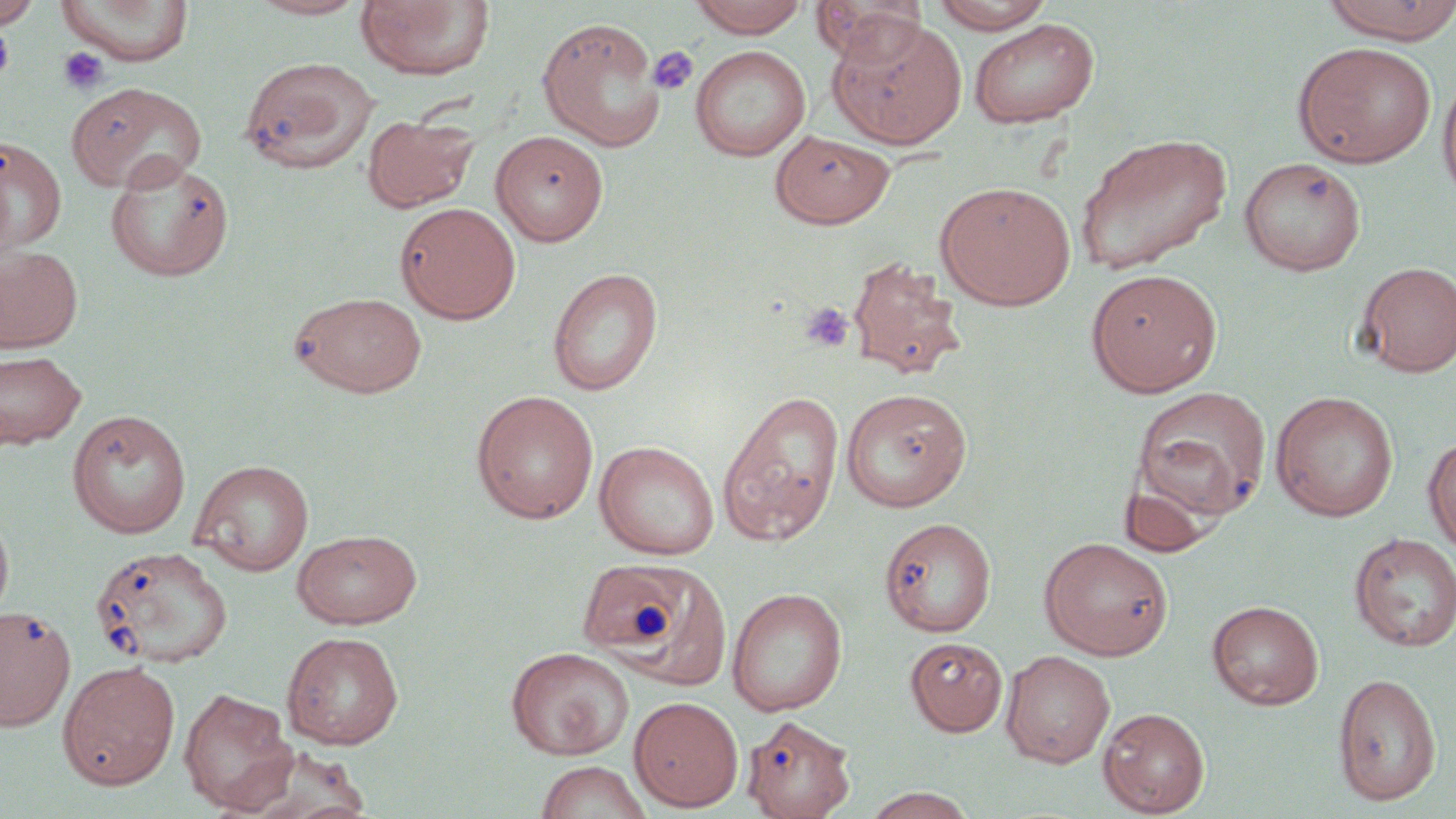

slide-level diagnosis = negative for blood parasites
uninfected red blood cell locations (subset) = approximate bounding boxes as (x1,y1)-(x2,y2) corner pairs in pixels: (0,0)-(43,28), (245,0)-(372,20), (687,0)-(810,38), (811,0)-(928,66), (929,0)-(1058,33), (1319,0)-(1456,45), (56,1)-(195,66), (355,1)-(495,82), (827,14)-(968,150), (536,16)-(666,152), (968,18)-(1099,128), (1293,41)-(1437,168), (690,45)-(811,161), (240,56)-(379,174), (1438,70)-(1456,208), (67,81)-(207,193), (363,114)-(479,211), (490,130)-(608,246), (770,130)-(895,228), (1075,132)-(1233,274), (0,136)-(66,254), (105,154)-(236,282), (1239,156)-(1366,275), (935,181)-(1076,310), (395,202)-(521,323), (0,244)-(83,353), (846,255)-(965,379), (1355,261)-(1456,377), (547,267)-(663,396), (1085,268)-(1223,396), (288,291)-(428,398), (0,350)-(86,449), (840,387)-(972,512), (1131,387)-(1272,523), (470,390)-(600,524), (717,390)-(844,545), (1269,391)-(1400,522), (66,409)-(192,539), (1423,433)-(1456,557), (594,440)-(719,560), (190,459)-(314,575), (0,503)-(15,628), (879,517)-(997,637), (292,529)-(423,629), (1349,532)-(1456,652), (1039,537)-(1173,660), (90,545)-(234,669), (579,559)-(733,690), (726,587)-(848,717), (1207,599)-(1324,709), (0,605)-(76,731), (282,631)-(404,749), (905,636)-(1008,736), (506,646)-(634,760), (1000,649)-(1116,768), (57,661)-(181,790), (1333,673)-(1442,806), (179,687)-(298,814), (629,696)-(744,812), (1098,707)-(1210,816), (743,714)-(857,819), (228,747)-(377,819), (533,759)-(653,819), (860,786)-(981,819)
modality = light microscopy
image size = 1456×819 pixels
stain = May-Grünwald-Giemsa
preparation = thin blood smear
platelet locations (subset) = approximate bounding boxes as (x1,y1)-(x2,y2) corner pairs in pixels: (648,46)-(699,96), (58,47)-(109,95), (799,302)-(855,353)
field of view = one of a larger specimen
magnification = 1000x